Point out each leukocyte.
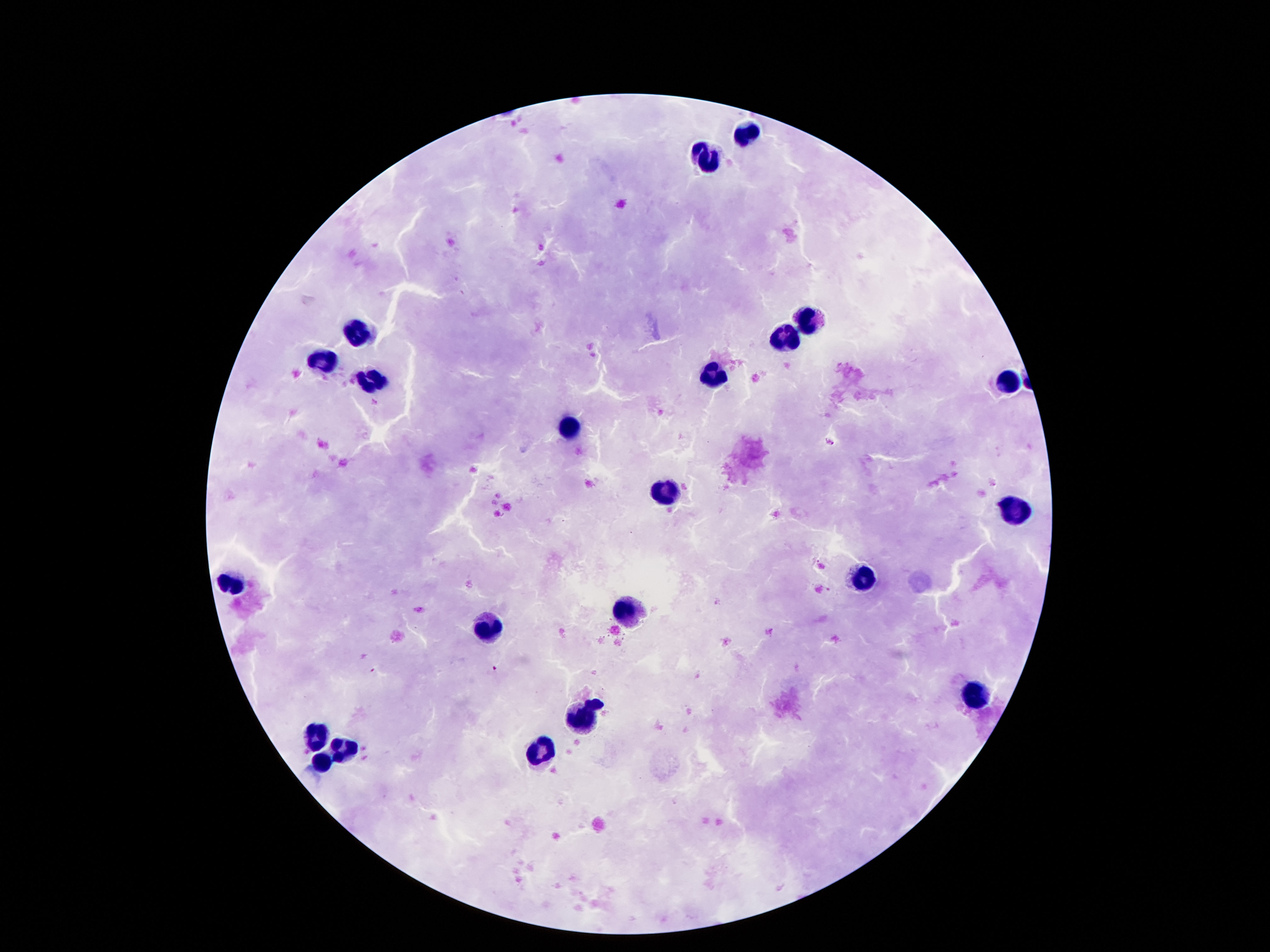
Approximate object centers, in pixels from the top-left corner.
Leukocytes: (x=743, y=133), (x=709, y=157), (x=803, y=318), (x=360, y=330), (x=787, y=334), (x=323, y=360), (x=712, y=377), (x=1006, y=381), (x=371, y=383), (x=570, y=427), (x=667, y=490), (x=1014, y=509), (x=869, y=577), (x=234, y=584), (x=628, y=613), (x=486, y=631), (x=972, y=695), (x=583, y=720), (x=318, y=734), (x=343, y=750), (x=537, y=753), (x=321, y=760).

{
  "preparation": "thick blood smear",
  "field_of_view": "single",
  "image_size": "1270×952 pixels",
  "magnification": "100x",
  "capture": "smartphone camera through the microscope eyepiece",
  "patient_malaria_status": "negative",
  "stain": "Giemsa"
}